State which parasite is depicted.
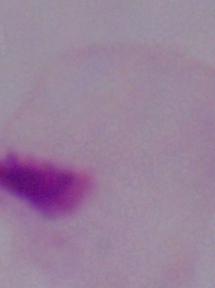
This is a trichomonad.

Summary:
  - Modality: photomicrograph
  - Magnification: 1000x